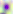

400x magnification. Photomicrograph. Toxoplasma gondii is seen.